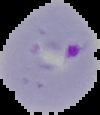

image type = segmented cell region on a black background
preparation = thin blood smear
image size = 100×115 pixels
result = Plasmodium parasites detected